Report the malaria status of this cell.
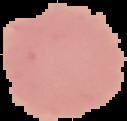
It is uninfected.

image type = cell region segmented out of the field of view; surrounding area masked to black
image size = 127×121 pixels
preparation = thin blood smear